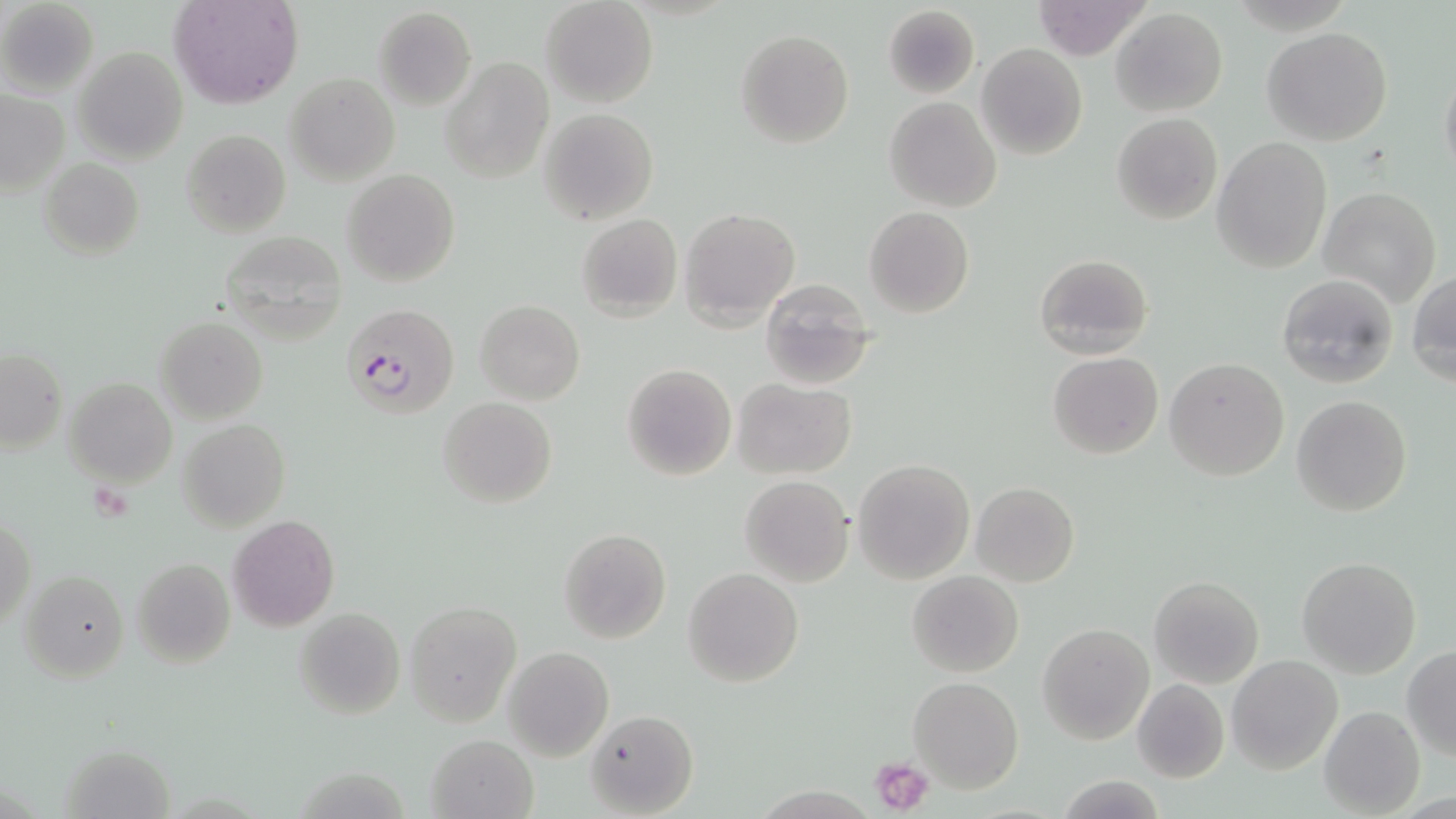

Summary:
  - Coordinate format: approximate bounding boxes as (x1, y1, x2, y2) in pixels
  - Platelet locations: (872, 756, 937, 816)
  - Plasmodium falciparum-infected red blood cell locations: (341, 303, 461, 420)
  - Uninfected red blood cell locations: (171, 0, 302, 108), (541, 0, 658, 108), (0, 1, 99, 96), (1032, 1, 1152, 59), (882, 4, 979, 99), (373, 7, 476, 108), (1111, 8, 1228, 115), (1262, 26, 1394, 146), (735, 29, 854, 147), (976, 43, 1088, 162), (74, 47, 187, 165), (441, 57, 553, 184), (1439, 57, 1456, 187), (286, 74, 399, 186), (0, 90, 68, 194), (885, 96, 1001, 211), (539, 108, 658, 225), (1111, 112, 1223, 224), (1153, 120, 1287, 243), (181, 129, 292, 238), (1211, 137, 1333, 272), (40, 158, 144, 260), (342, 168, 461, 288), (1318, 187, 1442, 307), (864, 206, 974, 318), (680, 208, 799, 328), (576, 214, 682, 321), (217, 232, 347, 342), (1033, 253, 1153, 360), (1408, 269, 1456, 385), (1275, 274, 1397, 388), (758, 279, 880, 389), (476, 299, 585, 405), (155, 316, 267, 424), (1, 348, 67, 452), (1047, 351, 1163, 459), (1164, 357, 1289, 481), (622, 363, 736, 480), (64, 379, 177, 487), (733, 379, 857, 479), (1291, 394, 1412, 518), (438, 397, 557, 508), (179, 419, 289, 532), (853, 459, 975, 584), (739, 475, 854, 586), (971, 481, 1079, 586), (227, 515, 339, 633), (1, 517, 34, 629), (557, 528, 671, 646), (1297, 556, 1421, 678), (131, 558, 235, 669), (683, 567, 803, 687), (906, 570, 1024, 677), (19, 571, 129, 682), (1148, 575, 1265, 688), (405, 601, 521, 726), (295, 608, 405, 719), (1037, 623, 1154, 746), (502, 647, 613, 761), (1402, 647, 1456, 759), (1227, 655, 1342, 773), (909, 677, 1023, 793), (1131, 679, 1229, 783), (1318, 705, 1426, 816), (585, 708, 698, 817), (427, 734, 538, 819), (1055, 775, 1169, 818)
  - Slide-level diagnosis: Plasmodium falciparum
  - Image size: 1456×819 pixels
  - Modality: optical microscopy
  - Magnification: 1000x
  - Preparation: thin blood film
  - Stain: May-Grünwald-Giemsa
  - Field of view: single